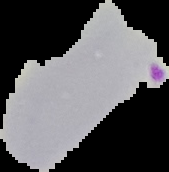
Summary:
  - Image type: segmented cell region with the area outside set to black
  - Malaria status: parasitized
  - Preparation: thin blood smear
  - Image size: 169×172 pixels